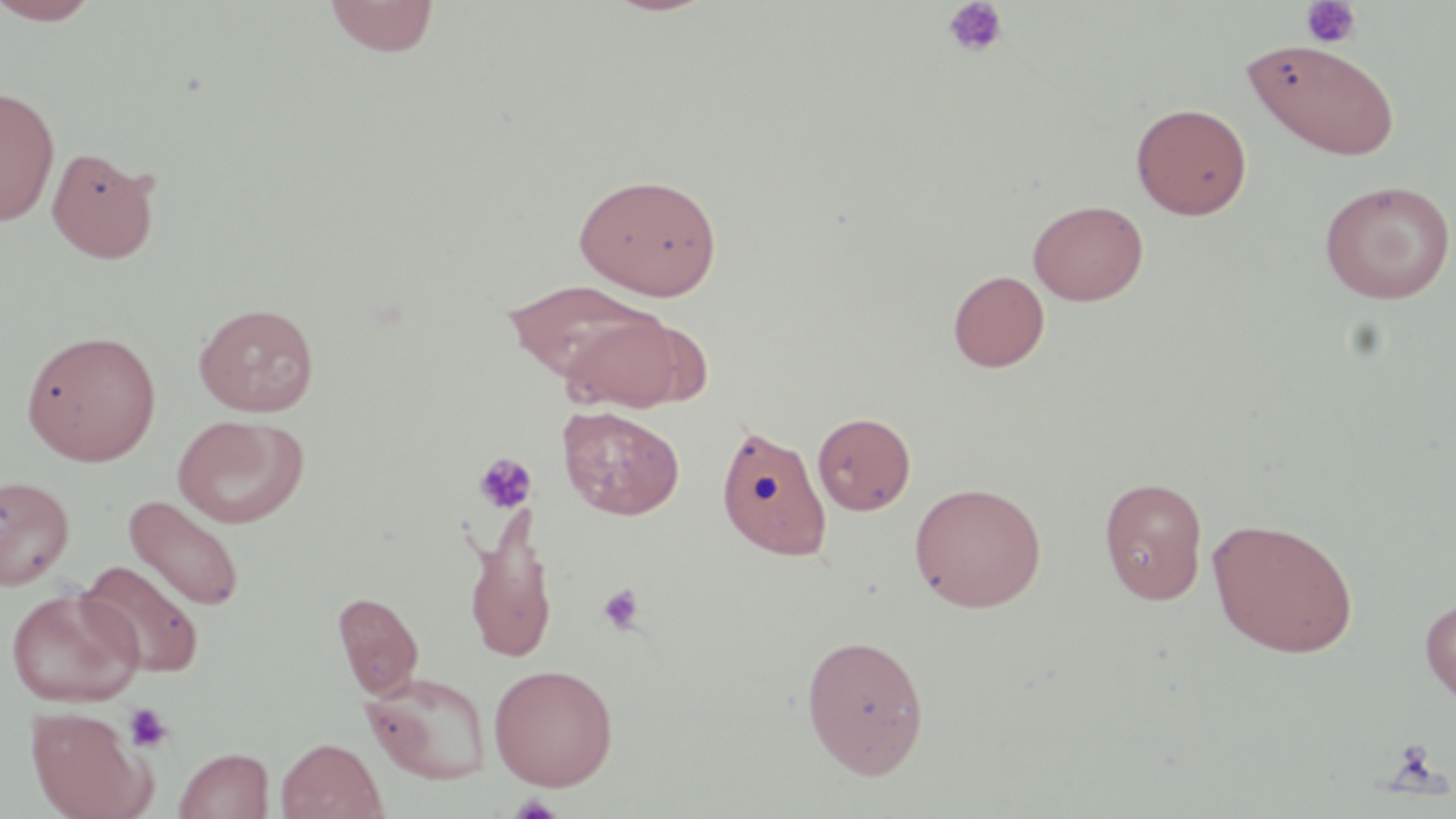
slide-level diagnosis = no evidence of blood parasites
image size = 1456×819 pixels
field of view = one of a larger specimen
platelet locations = approximate bounding boxes as (x1, y1, x2, y2) in pixels: (941, 0, 1009, 59), (1300, 1, 1362, 49), (473, 452, 536, 514), (597, 583, 645, 635), (123, 703, 174, 753), (1391, 740, 1437, 780), (508, 793, 563, 819)
stain = May-Grünwald-Giemsa
magnification = 1000x
modality = optical microscopy
uninfected red blood cell locations = approximate bounding boxes as (x1, y1, x2, y2) in pixels: (0, 0, 104, 26), (323, 0, 440, 58), (1241, 39, 1401, 161), (0, 84, 60, 227), (1131, 102, 1252, 219), (46, 146, 160, 264), (574, 171, 723, 299), (1319, 180, 1455, 304), (1028, 198, 1149, 306), (947, 270, 1050, 372), (503, 280, 664, 380), (193, 302, 320, 417), (558, 308, 707, 413), (21, 329, 161, 466), (557, 405, 685, 521), (812, 412, 916, 515), (171, 414, 309, 529), (715, 423, 833, 562), (0, 475, 75, 590), (1098, 476, 1208, 603), (908, 481, 1047, 612), (123, 495, 245, 612), (464, 504, 558, 666), (1207, 517, 1359, 658), (76, 560, 206, 678), (5, 587, 143, 707), (332, 591, 424, 699), (1419, 595, 1456, 707), (800, 633, 930, 778), (488, 663, 619, 790), (361, 670, 493, 785), (26, 706, 156, 819), (275, 736, 387, 819), (173, 746, 273, 819)
preparation = thin blood smear